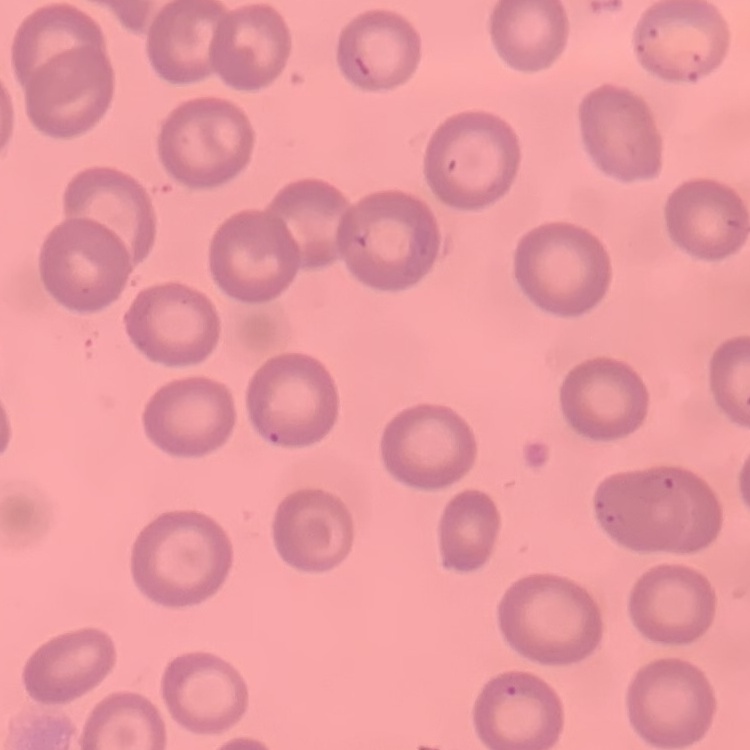
The erythrocytes exhibit no rouleaux formation. Thin blood smear. One tile cut from a larger photomicrograph. Stained with either Field's or Giemsa.